Mark where platelets are.
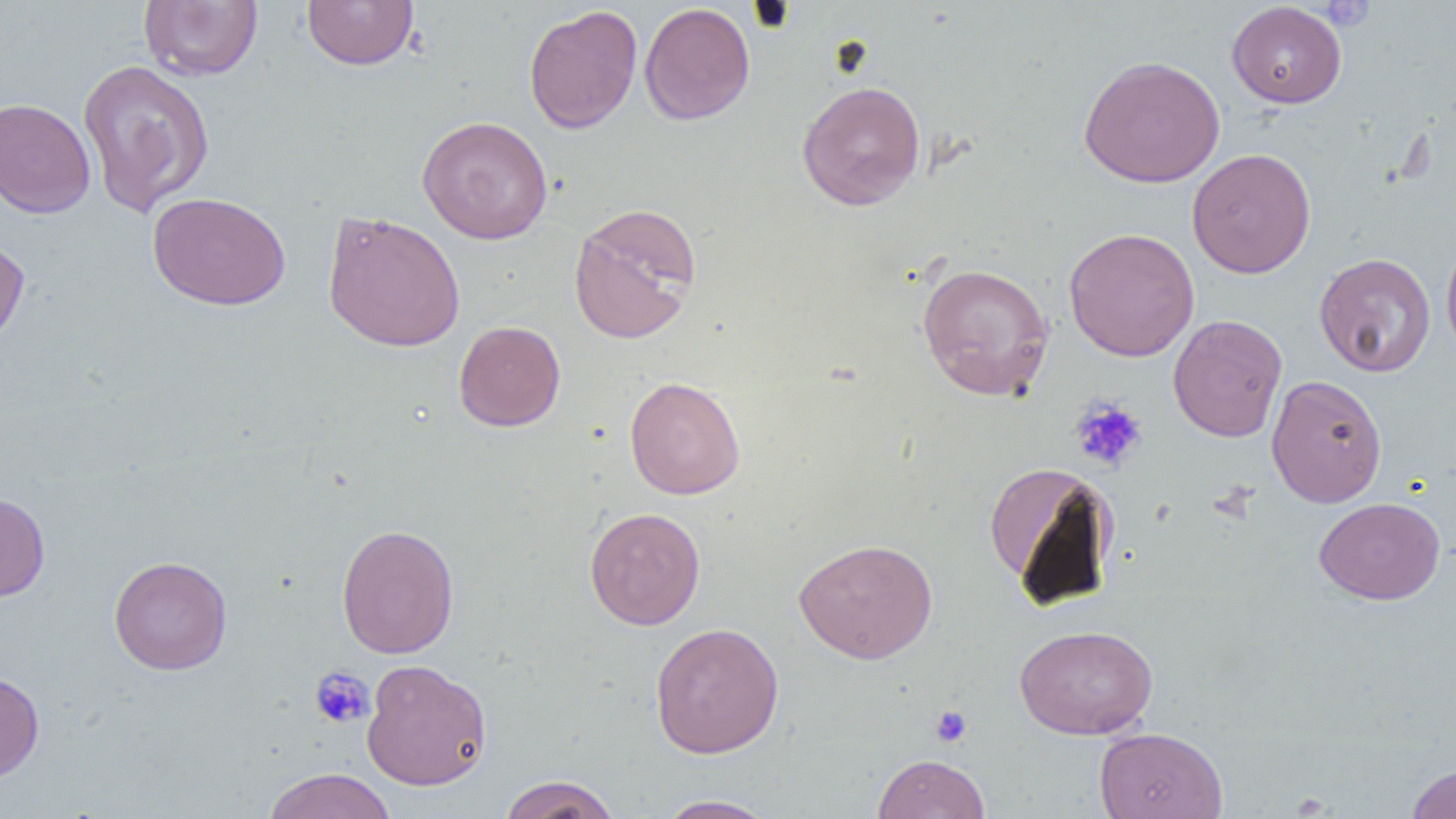
Approximate bounding boxes as (x1, y1, x2, y2) in pixels.
Platelets: (1320, 1, 1374, 31), (1070, 397, 1147, 472), (309, 667, 374, 729), (930, 705, 972, 747).

Uninfected red blood cell locations: (302, 0, 418, 70), (138, 1, 263, 81), (1226, 2, 1347, 108), (639, 3, 755, 126), (523, 5, 642, 134), (1078, 55, 1225, 188), (77, 59, 215, 218), (797, 80, 926, 211), (0, 97, 96, 218), (417, 115, 553, 244), (1187, 148, 1316, 278), (148, 191, 290, 310), (568, 202, 702, 345), (322, 210, 466, 353), (1064, 227, 1200, 361), (0, 230, 30, 351), (1440, 231, 1456, 364), (1314, 252, 1436, 377), (916, 262, 1054, 401), (1168, 314, 1287, 442), (453, 320, 566, 431), (1266, 374, 1387, 508), (624, 376, 745, 499), (984, 462, 1119, 605), (0, 491, 50, 601), (1315, 497, 1445, 605), (584, 506, 706, 630), (336, 524, 459, 659), (793, 537, 938, 664), (109, 555, 232, 675), (649, 622, 784, 758), (1014, 624, 1158, 739), (361, 659, 492, 790), (0, 671, 44, 783), (1094, 727, 1228, 819), (873, 753, 991, 818), (1405, 762, 1456, 819), (263, 768, 396, 819), (498, 774, 620, 819), (654, 794, 779, 818). Slide-level diagnosis: no evidence of blood parasites. Optical microscopy. Single field of view. Captured at 1000x magnification. Thin blood smear. Image is 1456×819 pixels.